Classify this cell by malaria status.
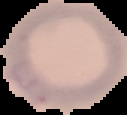

It is uninfected.

Summary:
  - Preparation: thin blood smear
  - Image type: segmented cell region with the area outside set to black
  - Image size: 127×115 pixels